Report the malaria status of this cell.
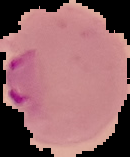

It is parasitized.

From a thin blood film. The area outside the segmented cell region is set to black. Image is 130×157 pixels.